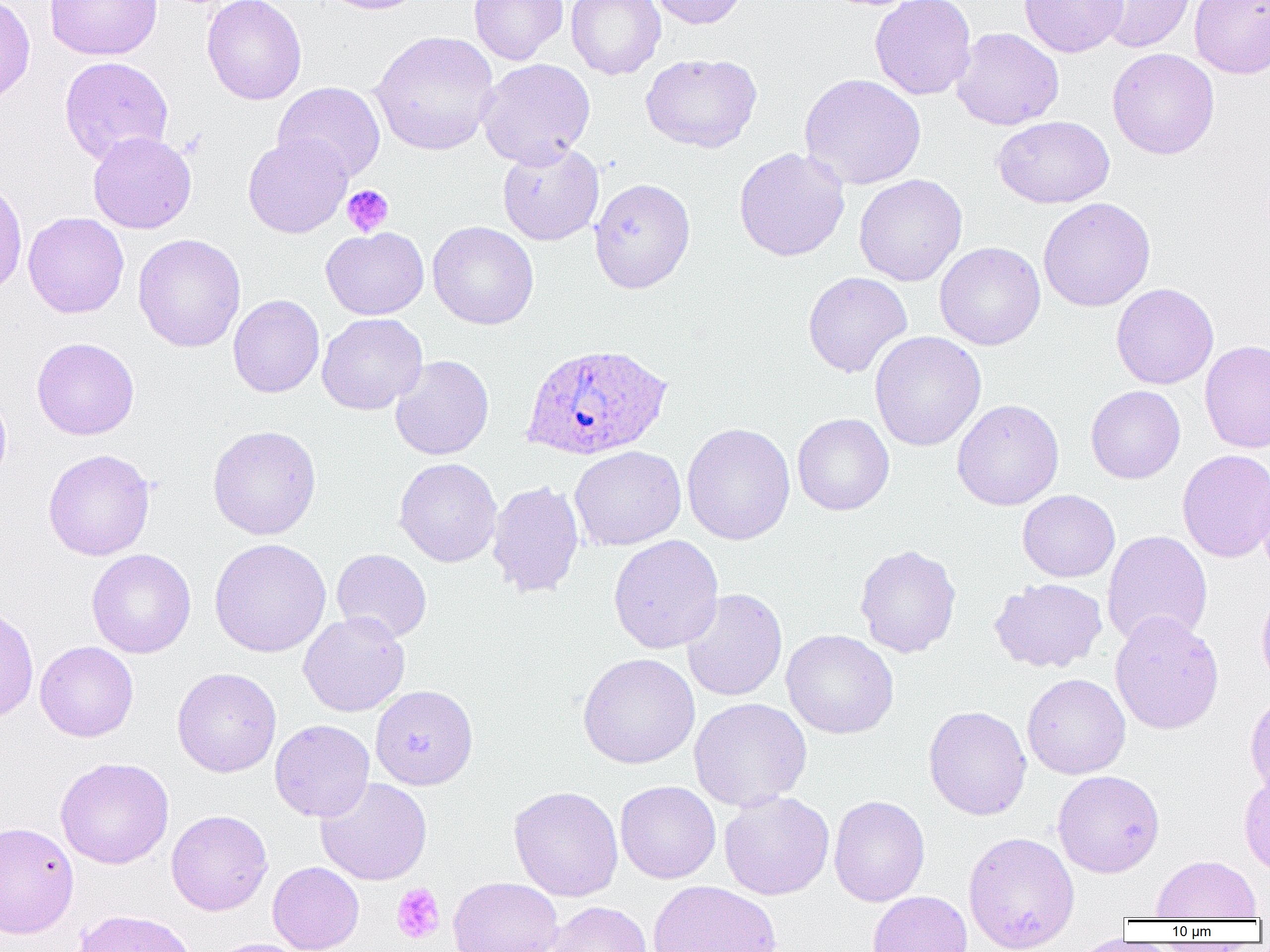

slide_level_diagnosis: Plasmodium ovale
field_of_view: single
magnification: 1000x
image_size: 1270×952 pixels
platelet_locations: 'approximate bounding boxes as (x1,y1)-(x2,y2) corner pairs in pixels: (342,185)-(394,237), (406,732)-(434,758), (391,883)-(445,944)'
modality: light microscopy
preparation: thin blood smear
uninfected_red_blood_cell_locations: 'approximate bounding boxes as (x1,y1)-(x2,y2) corner pairs in pixels: (0,0)-(35,106), (44,0)-(162,61), (201,0)-(306,105), (317,0)-(429,15), (469,0)-(568,65), (566,0)-(665,79), (645,0)-(749,29), (869,0)-(977,100), (1018,0)-(1128,58), (1088,0)-(1197,53), (1189,0)-(1270,79), (951,27)-(1064,130), (369,30)-(499,156), (1106,48)-(1220,160), (640,52)-(762,153), (59,56)-(174,164), (477,58)-(596,168), (799,73)-(926,190), (273,81)-(386,183), (992,115)-(1114,208), (87,131)-(197,234), (242,134)-(352,238), (497,141)-(604,245), (734,147)-(850,262), (854,174)-(967,286), (589,177)-(696,294), (0,181)-(27,298), (1038,197)-(1156,312), (22,212)-(129,318), (428,221)-(539,330), (321,227)-(429,320), (133,233)-(246,353), (934,241)-(1046,351), (802,271)-(912,378), (1111,282)-(1219,389), (228,295)-(324,398), (317,313)-(427,415), (869,331)-(986,451), (32,337)-(140,440), (1200,340)-(1270,453), (390,355)-(494,460), (1085,385)-(1185,484), (0,391)-(12,490), (951,398)-(1064,510), (792,413)-(894,516), (681,422)-(796,545), (207,424)-(322,540), (569,445)-(686,551), (43,448)-(155,560), (1177,449)-(1270,563), (394,457)-(502,567), (1255,465)-(1270,577), (486,480)-(585,599), (1018,489)-(1120,582), (1102,530)-(1213,648), (608,534)-(724,654), (208,538)-(331,658), (854,543)-(961,658), (331,548)-(432,643), (87,549)-(196,658), (989,578)-(1107,672), (1256,586)-(1270,695), (681,588)-(788,701), (0,604)-(39,723), (298,611)-(410,717), (1109,611)-(1224,735), (781,629)-(899,739), (35,641)-(139,742), (577,653)-(700,769), (172,667)-(282,778), (1022,673)-(1131,779), (370,684)-(479,790), (1244,690)-(1270,797), (689,697)-(812,811), (923,705)-(1031,820), (270,719)-(375,822), (55,757)-(174,869), (1238,769)-(1270,876), (1052,770)-(1165,878), (315,778)-(432,886), (615,780)-(721,884), (509,785)-(624,902), (719,790)-(834,900), (829,795)-(930,907), (166,809)-(272,915), (0,821)-(79,938), (963,831)-(1080,951), (1151,855)-(1262,920), (267,861)-(364,952), (448,876)-(563,952), (648,880)-(781,952), (867,891)-(972,952), (544,901)-(653,952), (71,909)-(200,952), (206,937)-(309,952)'
plasmodium_ovale_infected_red_blood_cell_locations: 'approximate bounding boxes as (x1,y1)-(x2,y2) corner pairs in pixels: (520,342)-(673,461)'